State the preparation type.
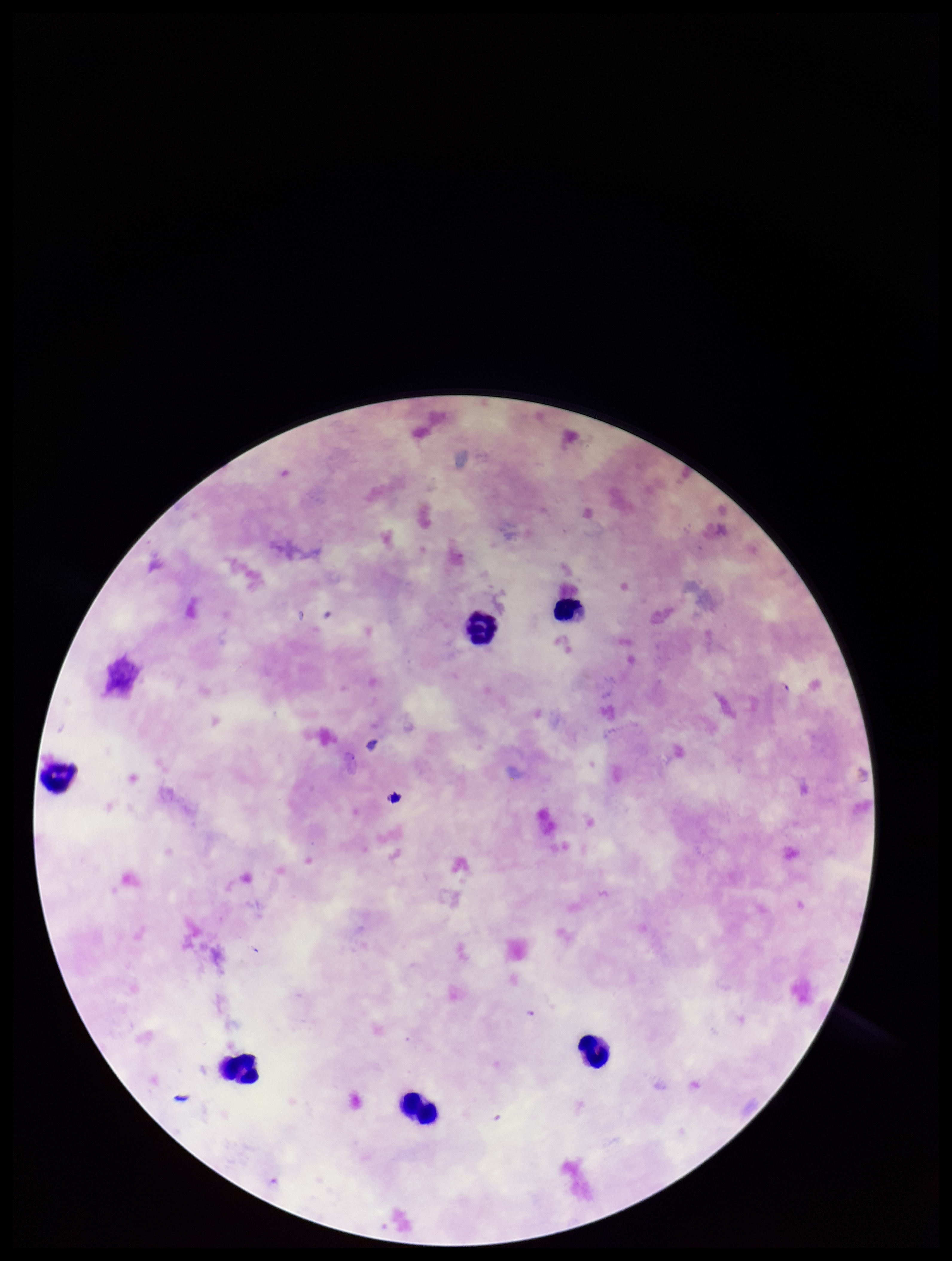

It is a thick blood smear.

Summary:
  - Leukocyte count: 6
  - Stain: Giemsa
  - Patient malaria status: infected
  - Parasite count: 0
  - Field of view: one from this slide
  - Capture: smartphone photograph through the microscope eyepiece
  - Species reported for this patient: Plasmodium falciparum
  - Image size: 952×1261 pixels
  - Plasmodium parasites: none identified